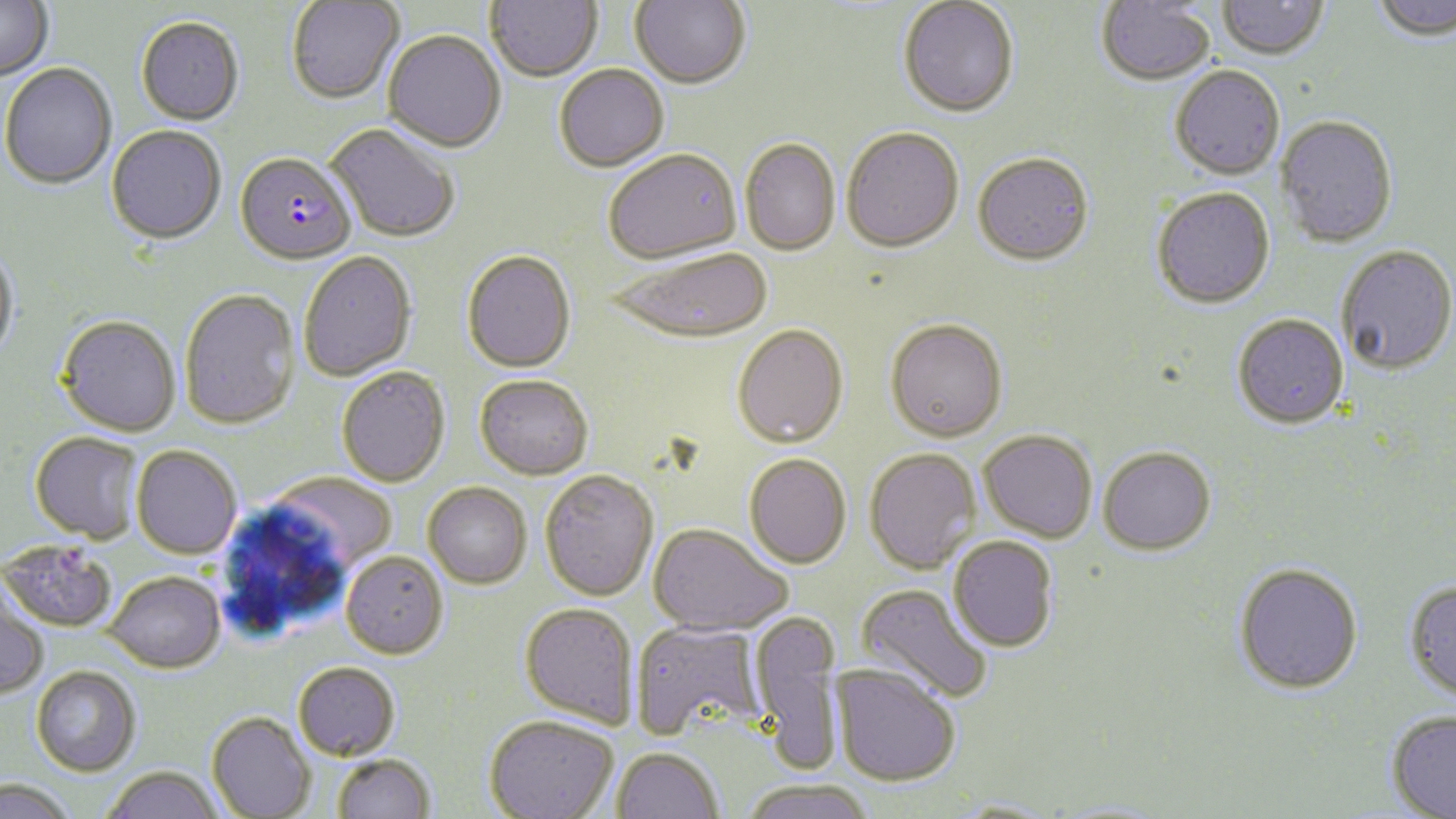

{
  "slide_level_diagnosis": "Plasmodium falciparum",
  "magnification": "1000x",
  "stain": "May-Grünwald-Giemsa",
  "uninfected_red_blood_cell_locations": "approximate bounding boxes as (x1,y1)-(x2,y2) corner pairs in pixels: (486,0)-(601,81), (898,0)-(1019,117), (1217,0)-(1328,62), (1370,0)-(1455,44), (0,1)-(54,81), (287,1)-(404,104), (630,1)-(751,89), (1097,1)-(1215,87), (136,15)-(245,125), (383,29)-(506,151), (0,63)-(118,190), (554,64)-(669,171), (1170,66)-(1285,181), (1275,115)-(1398,248), (326,124)-(460,243), (107,125)-(227,244), (841,126)-(964,252), (740,137)-(841,255), (603,148)-(742,263), (972,153)-(1094,266), (1151,188)-(1275,310), (0,245)-(20,364), (608,246)-(773,343), (1337,246)-(1456,376), (461,249)-(576,372), (298,251)-(417,381), (179,288)-(300,429), (57,314)-(181,436), (1232,314)-(1349,429), (885,318)-(1008,441), (733,324)-(848,447), (336,366)-(450,487), (475,374)-(593,479), (979,429)-(1097,542), (30,431)-(145,543), (131,445)-(242,559), (1098,446)-(1216,555), (864,447)-(982,574), (744,453)-(852,568), (540,469)-(659,600), (268,472)-(397,573), (423,482)-(532,588), (648,523)-(791,636), (949,535)-(1059,652), (1,540)-(118,633), (341,551)-(447,658), (1233,563)-(1363,693), (103,570)-(225,672), (1404,580)-(1456,703), (856,583)-(993,704), (0,587)-(49,699), (519,602)-(639,728), (749,610)-(844,774), (630,620)-(767,741), (293,661)-(400,760), (831,663)-(960,787), (31,665)-(141,776), (1386,710)-(1456,817), (206,711)-(315,818), (484,715)-(618,819), (612,747)-(723,819), (332,753)-(436,819), (101,766)-(225,819), (1,778)-(76,819), (740,779)-(876,819), (945,798)-(1065,818)",
  "plasmodium_falciparum_infected_red_blood_cell_locations": "approximate bounding boxes as (x1,y1)-(x2,y2) corner pairs in pixels: (236,151)-(356,264)",
  "image_size": "1456×819 pixels",
  "modality": "optical microscopy",
  "preparation": "thin blood smear",
  "field_of_view": "one of a larger specimen"
}